Comment on the morphology of the red blood cells.
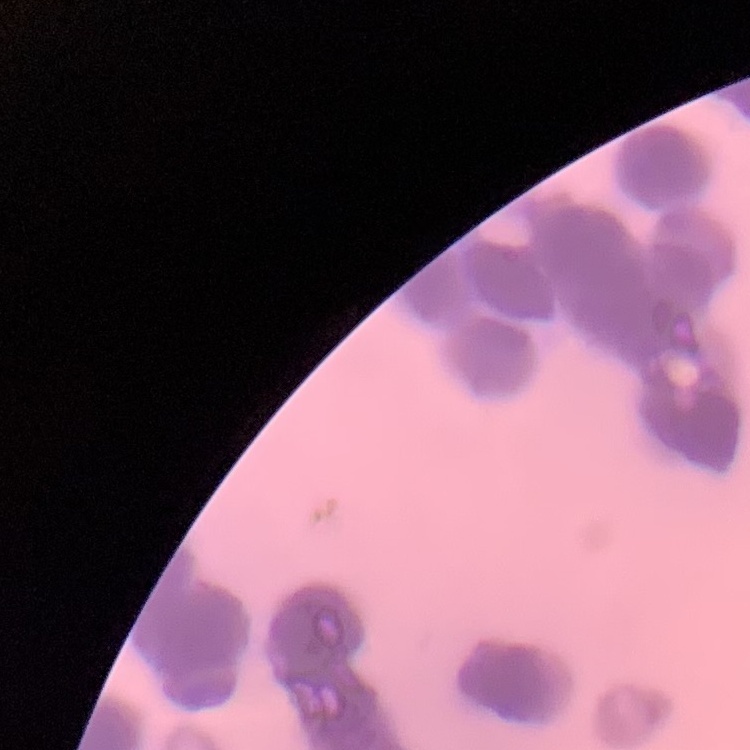
They show rouleaux formation.

Summary:
  - Stain: Field's or Giemsa
  - Preparation: thin peripheral smear
  - Image type: one tile cut from a larger photomicrograph